Outline each blood parasite and name the species.
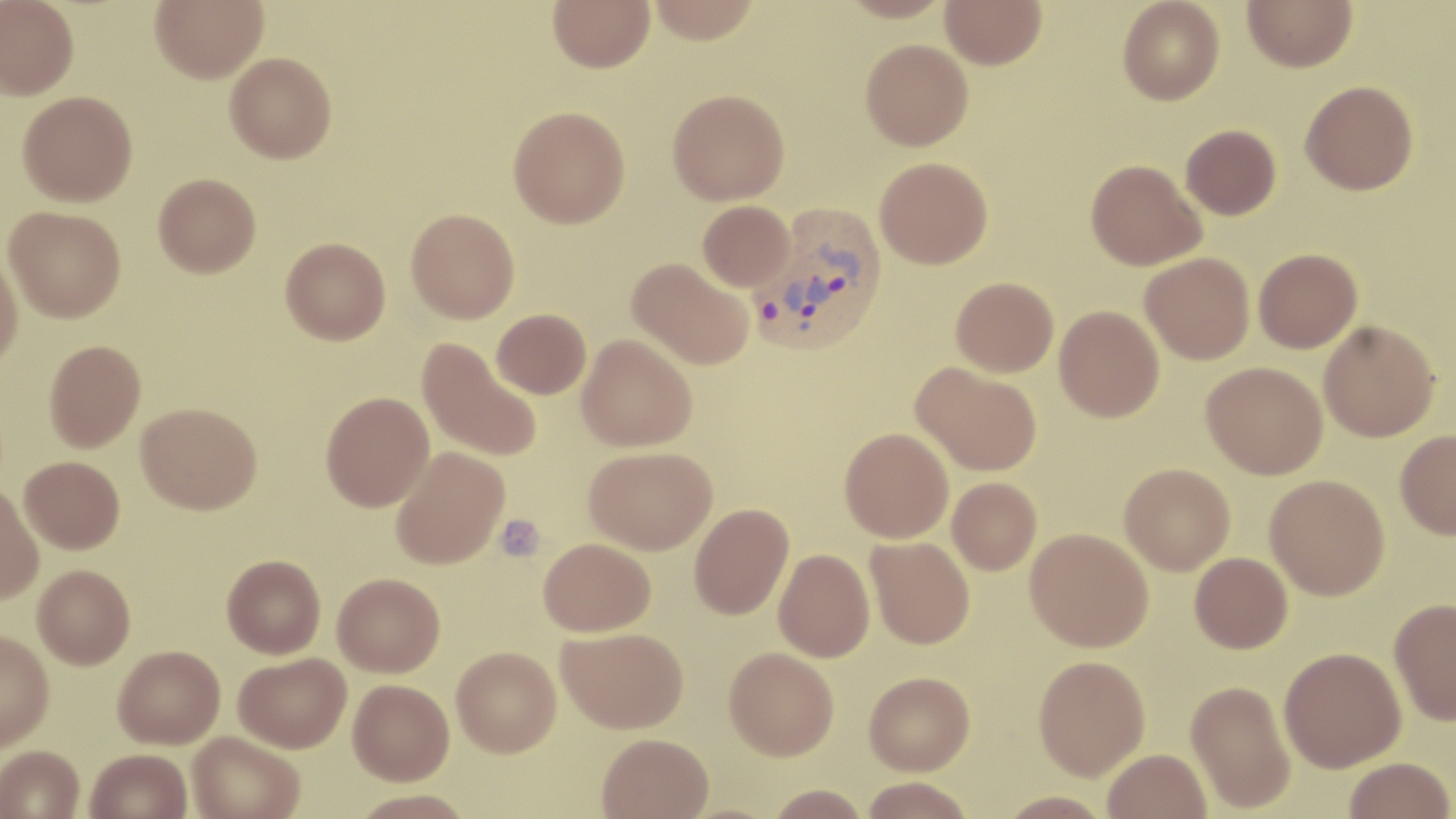
Approximate bounding boxes as named x1/y1/x2/y2 corners in pixels.
Plasmodium vivax-infected red blood cells: (x1=749, y1=205, x2=889, y2=359).
No Plasmodium falciparum, Plasmodium ovale, Plasmodium malariae, Babesia divergens, or Trypanosoma brucei observed.

Uninfected red blood cell locations: (x1=0, y1=0, x2=79, y2=99), (x1=150, y1=0, x2=268, y2=82), (x1=548, y1=0, x2=654, y2=72), (x1=647, y1=0, x2=762, y2=43), (x1=838, y1=0, x2=953, y2=23), (x1=940, y1=0, x2=1046, y2=69), (x1=1117, y1=0, x2=1224, y2=105), (x1=1242, y1=0, x2=1357, y2=72), (x1=860, y1=39, x2=973, y2=150), (x1=225, y1=52, x2=337, y2=163), (x1=1300, y1=80, x2=1418, y2=195), (x1=667, y1=88, x2=789, y2=205), (x1=18, y1=91, x2=137, y2=206), (x1=508, y1=105, x2=630, y2=228), (x1=1180, y1=124, x2=1281, y2=220), (x1=875, y1=156, x2=993, y2=268), (x1=1086, y1=159, x2=1206, y2=270), (x1=153, y1=173, x2=261, y2=278), (x1=697, y1=200, x2=794, y2=291), (x1=3, y1=205, x2=126, y2=322), (x1=406, y1=208, x2=519, y2=323), (x1=280, y1=237, x2=390, y2=344), (x1=0, y1=248, x2=24, y2=369), (x1=1253, y1=248, x2=1362, y2=353), (x1=1140, y1=253, x2=1255, y2=364), (x1=627, y1=257, x2=754, y2=370), (x1=951, y1=276, x2=1058, y2=377), (x1=1054, y1=305, x2=1164, y2=422), (x1=491, y1=309, x2=591, y2=399), (x1=1318, y1=320, x2=1440, y2=442), (x1=577, y1=334, x2=697, y2=451), (x1=417, y1=338, x2=542, y2=463), (x1=44, y1=340, x2=146, y2=451), (x1=1202, y1=361, x2=1328, y2=479), (x1=912, y1=362, x2=1043, y2=476), (x1=320, y1=391, x2=434, y2=511), (x1=136, y1=402, x2=262, y2=514), (x1=840, y1=427, x2=954, y2=543), (x1=1395, y1=429, x2=1456, y2=539), (x1=391, y1=446, x2=510, y2=569), (x1=583, y1=446, x2=717, y2=554), (x1=19, y1=455, x2=125, y2=553), (x1=1119, y1=463, x2=1235, y2=575), (x1=1264, y1=474, x2=1390, y2=600), (x1=947, y1=477, x2=1041, y2=575), (x1=0, y1=484, x2=44, y2=604), (x1=689, y1=503, x2=794, y2=620), (x1=1025, y1=528, x2=1153, y2=652), (x1=866, y1=536, x2=975, y2=649), (x1=538, y1=537, x2=656, y2=636), (x1=773, y1=549, x2=875, y2=662), (x1=1189, y1=552, x2=1292, y2=653), (x1=222, y1=554, x2=326, y2=658), (x1=33, y1=564, x2=135, y2=669), (x1=333, y1=572, x2=445, y2=677), (x1=1390, y1=598, x2=1456, y2=726), (x1=557, y1=626, x2=689, y2=733), (x1=0, y1=630, x2=54, y2=751), (x1=113, y1=644, x2=225, y2=748), (x1=451, y1=646, x2=561, y2=757), (x1=1279, y1=646, x2=1406, y2=772), (x1=724, y1=647, x2=839, y2=760), (x1=234, y1=652, x2=351, y2=753), (x1=1033, y1=655, x2=1150, y2=780), (x1=864, y1=671, x2=975, y2=775), (x1=348, y1=678, x2=454, y2=785), (x1=1185, y1=679, x2=1296, y2=814), (x1=188, y1=731, x2=305, y2=819), (x1=596, y1=732, x2=714, y2=819), (x1=0, y1=745, x2=84, y2=819), (x1=1103, y1=748, x2=1212, y2=819), (x1=86, y1=749, x2=192, y2=819), (x1=1344, y1=757, x2=1454, y2=818), (x1=858, y1=776, x2=977, y2=819), (x1=766, y1=784, x2=871, y2=819), (x1=996, y1=790, x2=1113, y2=818). Platelet locations: (x1=494, y1=513, x2=545, y2=561). Slide-level diagnosis: Plasmodium vivax. Light microscopy. May-Grünwald-Giemsa-stained preparation. One field of a larger specimen. Thin blood film. Captured at 1000x magnification. Image is 1456×819 pixels.